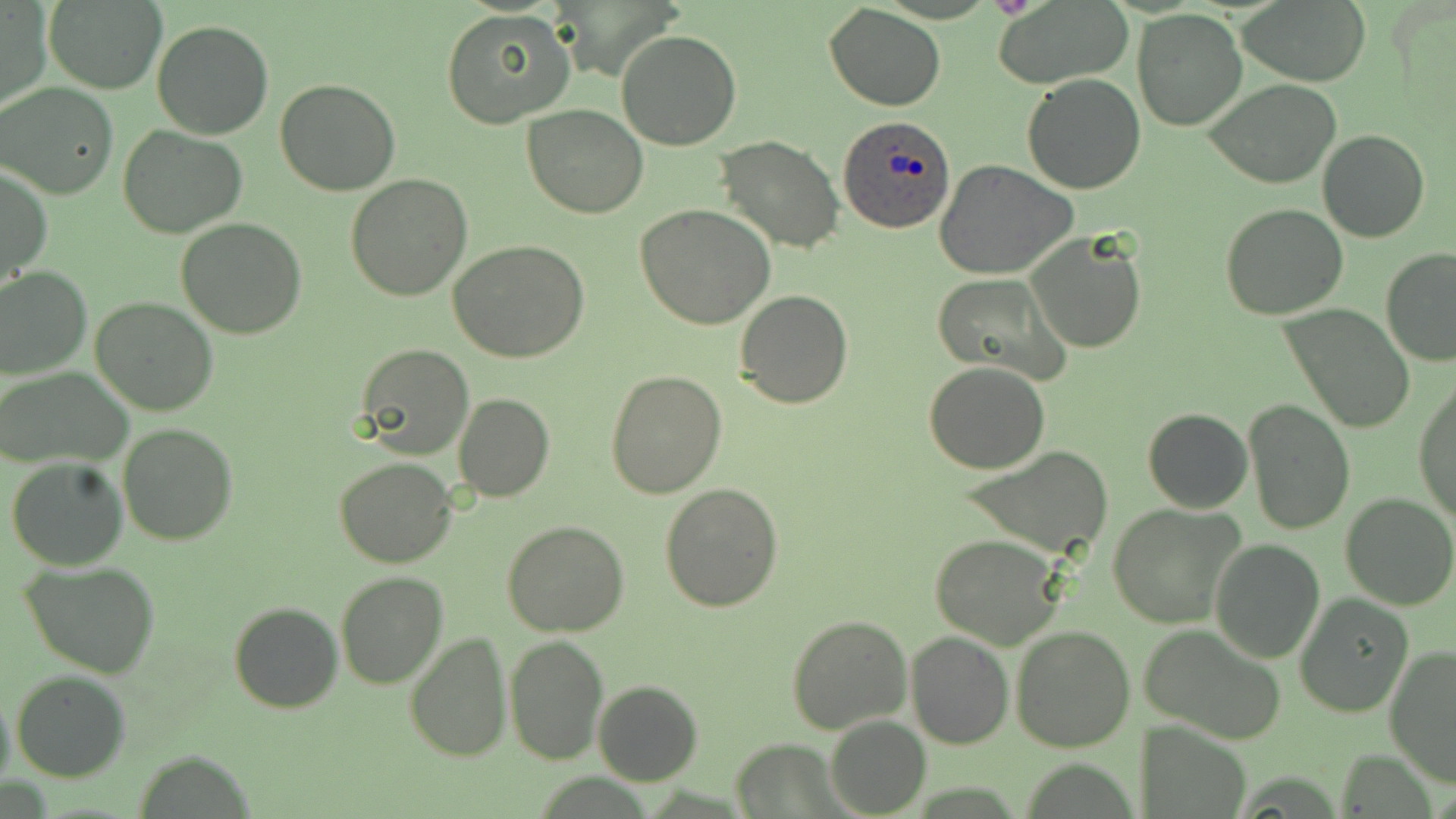

slide-level diagnosis = Plasmodium ovale
stain = May-Grünwald-Giemsa
uninfected red blood cell locations = approximate bounding boxes as (x1,y1)-(x2,y2) corner pairs in pixels: (994,0)-(1135,89), (1235,0)-(1371,85), (0,2)-(50,111), (41,3)-(165,92), (824,5)-(946,111), (440,7)-(575,130), (1131,9)-(1246,131), (151,18)-(274,139), (615,28)-(744,151), (1022,72)-(1146,193), (1204,78)-(1343,189), (275,79)-(401,196), (0,82)-(120,200), (522,105)-(649,218), (118,125)-(247,238), (1318,129)-(1430,244), (716,136)-(844,255), (937,163)-(1078,279), (1,167)-(51,290), (345,173)-(473,300), (1221,202)-(1349,319), (634,203)-(775,330), (175,217)-(307,339), (1026,233)-(1147,353), (449,240)-(592,364), (1380,250)-(1456,368), (0,267)-(92,379), (932,272)-(1067,380), (735,289)-(853,408), (90,297)-(219,417), (1281,304)-(1414,433), (355,344)-(473,461), (923,362)-(1052,475), (0,365)-(133,469), (605,370)-(725,498), (1414,374)-(1456,527), (453,394)-(554,503), (1242,400)-(1356,537), (1143,407)-(1253,513), (116,423)-(239,547), (958,446)-(1116,559), (7,455)-(129,571), (334,456)-(456,569), (659,482)-(783,612), (1340,493)-(1455,610), (1106,503)-(1246,629), (503,521)-(630,637), (929,534)-(1063,649), (1210,540)-(1325,662), (22,562)-(160,680), (335,572)-(449,691), (1294,595)-(1412,717), (228,601)-(343,714), (786,612)-(912,734), (1010,625)-(1137,752), (1140,625)-(1288,743), (907,631)-(1012,748), (405,633)-(511,762), (504,634)-(608,766), (1384,643)-(1456,786), (11,671)-(129,781), (591,679)-(703,786), (0,690)-(14,794), (826,715)-(930,818), (733,738)-(844,816)
image size = 1456×819 pixels
Plasmodium ovale-infected red blood cell locations = approximate bounding boxes as (x1,y1)-(x2,y2) corner pairs in pixels: (840,115)-(955,234)
magnification = 1000x
modality = light microscopy
field of view = single
preparation = thin blood smear